Name the parasite shown.
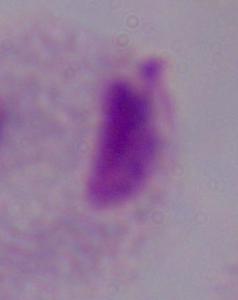

This is a trichomonad.

Summary:
  - Magnification: 1000x
  - Modality: micrograph